Identify the parasite.
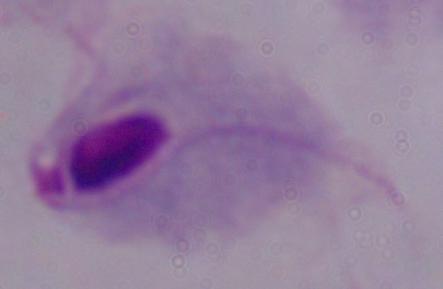

A trichomonad.

magnification = 1000x
modality = photomicrograph